Point out Plasmodium parasites and leukocytes.
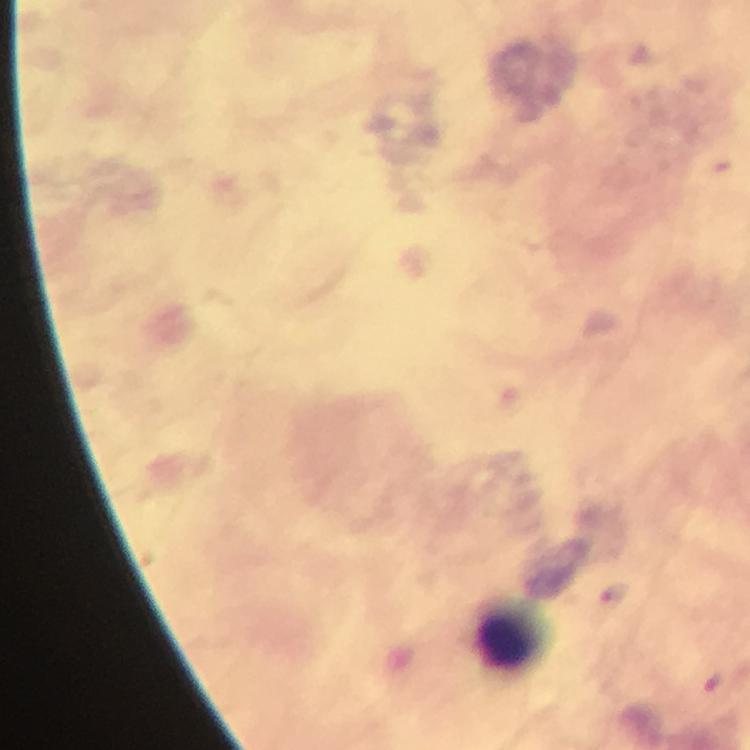

Approximate centers as (x, y) in pixels.
Plasmodium parasites: (614, 597).
Leukocytes: (508, 639).

Immersion oil applied. From a diagnostic examination for malaria. 100x magnification. Thick blood film. Cropped region of a single field of view. Image is 750×750 pixels. Giemsa-stained preparation. Smartphone photograph taken through a microscope.